Locate and identify every blood parasite.
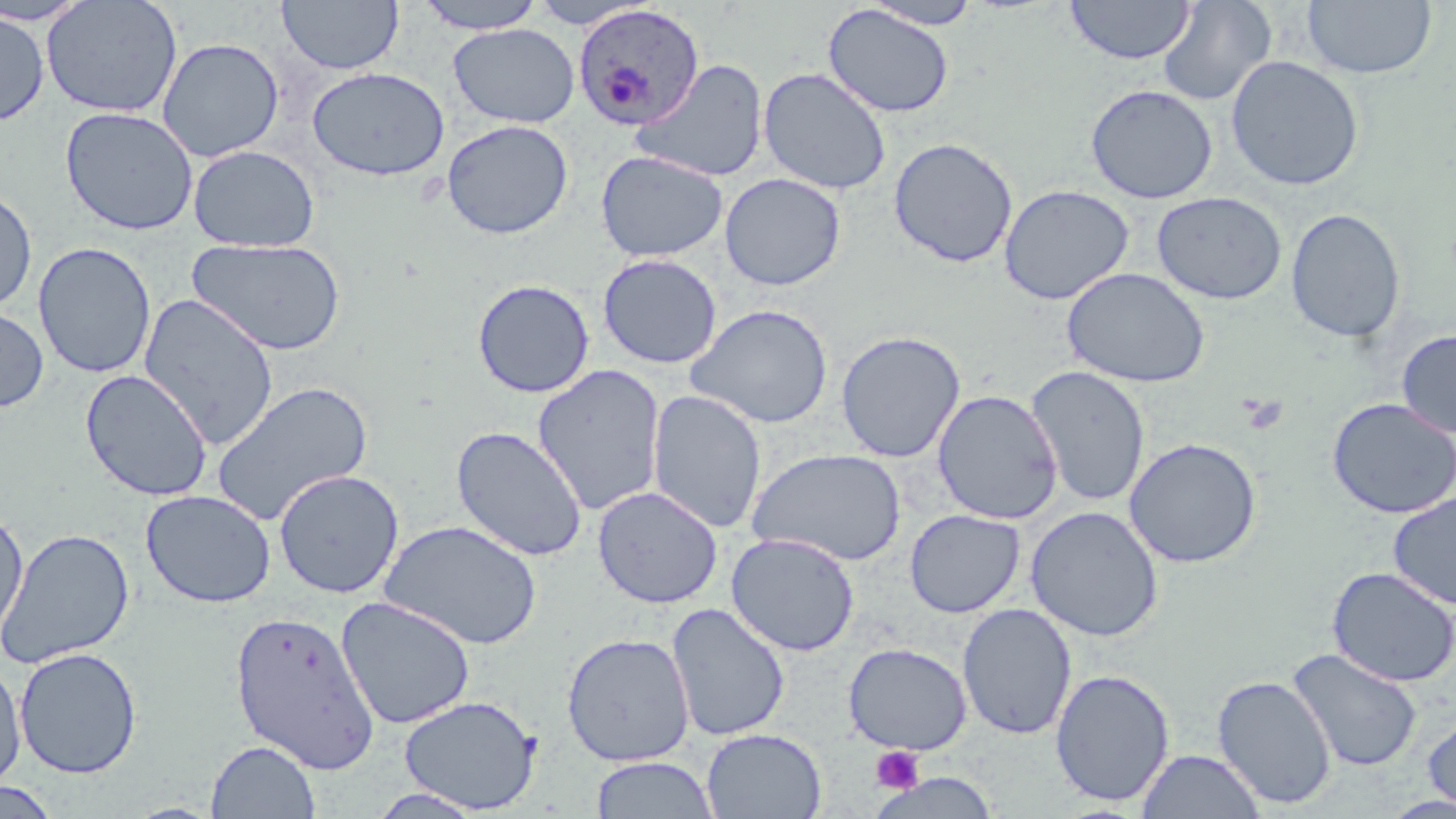
Approximate bounding boxes as [x1, y1, x2, y2] in pixels.
Plasmodium ovale-infected red blood cells: [572, 3, 704, 131].
No Plasmodium falciparum, Plasmodium malariae, Plasmodium vivax, Babesia divergens, or Trypanosoma brucei observed.

slide-level diagnosis = Plasmodium ovale
preparation = thin blood smear
magnification = 1000x
field of view = one of a larger specimen
stain = May-Grünwald-Giemsa
uninfected red blood cell locations = approximate bounding boxes as [x1, y1, x2, y2] in pixels: [41, 0, 183, 118], [276, 0, 404, 75], [413, 0, 549, 34], [528, 0, 655, 29], [1064, 0, 1196, 65], [0, 1, 93, 26], [862, 1, 986, 29], [1157, 1, 1277, 107], [1302, 1, 1436, 80], [823, 4, 954, 118], [0, 10, 50, 126], [448, 23, 579, 128], [157, 37, 284, 162], [1226, 55, 1364, 191], [630, 59, 769, 183], [307, 67, 449, 181], [758, 67, 892, 195], [1085, 84, 1218, 204], [60, 106, 198, 235], [441, 119, 574, 239], [889, 137, 1018, 268], [187, 144, 320, 252], [595, 150, 728, 262], [720, 173, 846, 291], [999, 184, 1134, 305], [0, 186, 37, 313], [1151, 191, 1287, 305], [1285, 208, 1406, 343], [186, 237, 347, 356], [33, 241, 157, 379], [597, 253, 722, 369], [1061, 267, 1210, 388], [472, 279, 595, 398], [138, 293, 280, 450], [0, 303, 51, 414], [685, 303, 834, 429], [1396, 328, 1456, 438], [835, 330, 966, 463], [532, 364, 666, 516], [1025, 365, 1151, 507], [79, 369, 214, 501], [212, 380, 373, 526], [647, 389, 767, 533], [932, 389, 1063, 524], [1326, 397, 1455, 519], [451, 425, 587, 562], [1124, 437, 1262, 568], [748, 447, 907, 566], [274, 469, 404, 598], [592, 486, 723, 608], [141, 489, 276, 608], [1388, 491, 1456, 610], [1025, 504, 1164, 642], [0, 505, 29, 642], [904, 509, 1025, 618], [381, 519, 542, 651], [0, 527, 135, 669], [726, 532, 860, 656], [1327, 567, 1456, 687], [335, 596, 475, 729], [666, 602, 791, 742], [957, 602, 1077, 740], [228, 608, 382, 774], [561, 632, 695, 767], [843, 642, 972, 755], [14, 647, 142, 779], [1287, 647, 1423, 772], [0, 660, 26, 792], [1050, 667, 1175, 807], [1212, 674, 1337, 809], [399, 695, 542, 813], [1422, 710, 1456, 813], [701, 728, 826, 818], [206, 740, 321, 818], [1137, 749, 1265, 818], [590, 755, 719, 818], [870, 770, 1000, 819], [0, 780, 61, 819], [366, 788, 489, 818]
modality = light microscopy
image size = 1456×819 pixels
platelet locations = approximate bounding boxes as [x1, y1, x2, y2] in pixels: [869, 746, 925, 794]